Give the extent of all Plasmodium malariae-infected red blood cells.
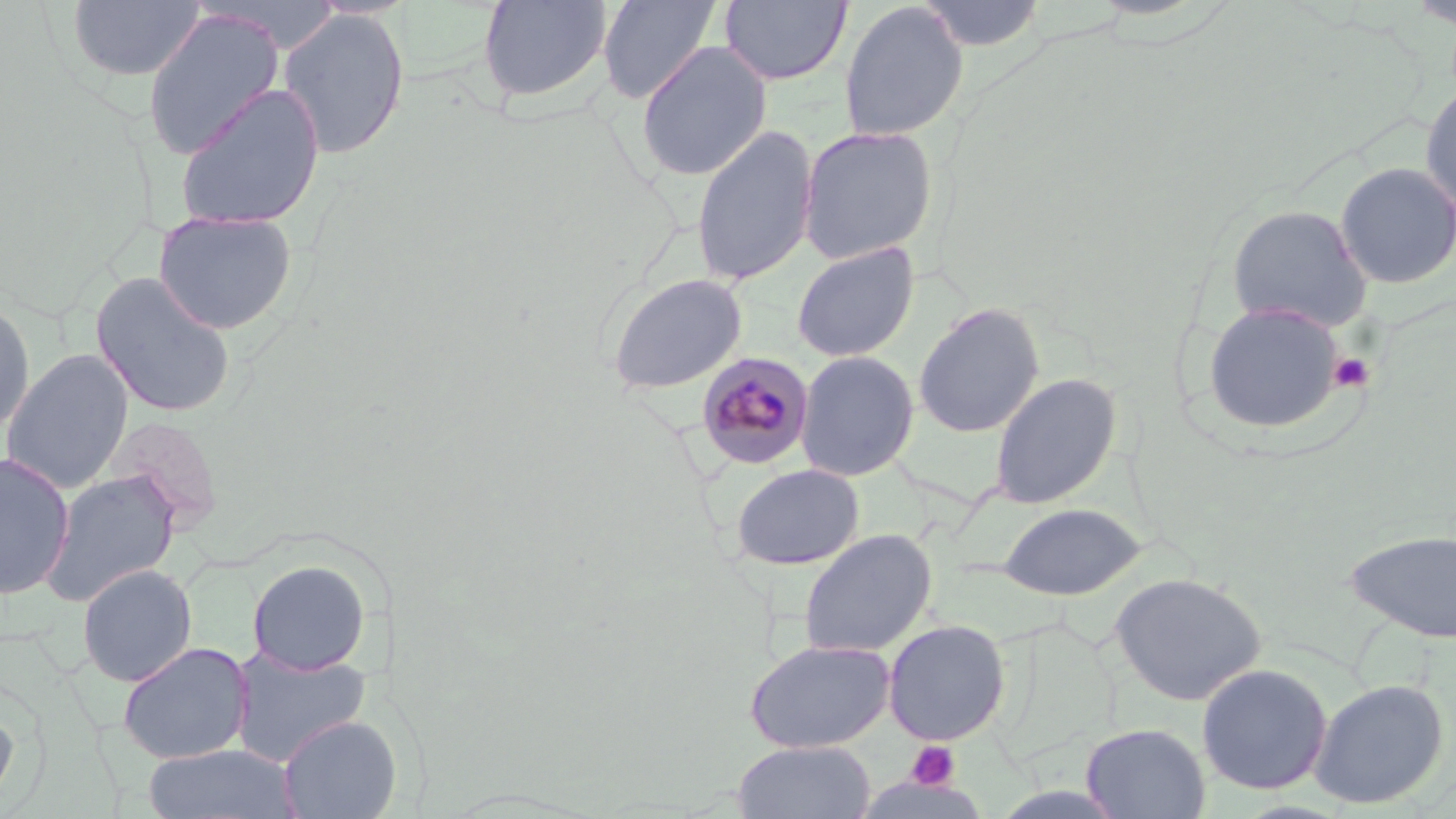

Approximate bounding boxes as named x1/y1/x2/y2 corners in pixels.
Plasmodium malariae-infected red blood cells: (x1=696, y1=351, x2=815, y2=470).

Summary:
  - Platelet locations: (x1=1328, y1=352, x2=1375, y2=393), (x1=906, y1=741, x2=961, y2=790)
  - Uninfected red blood cell locations: (x1=477, y1=0, x2=613, y2=105), (x1=596, y1=0, x2=723, y2=103), (x1=719, y1=0, x2=852, y2=86), (x1=918, y1=0, x2=1047, y2=52), (x1=66, y1=1, x2=206, y2=83), (x1=838, y1=1, x2=969, y2=142), (x1=277, y1=7, x2=410, y2=159), (x1=141, y1=8, x2=284, y2=160), (x1=635, y1=42, x2=773, y2=181), (x1=1420, y1=79, x2=1456, y2=215), (x1=173, y1=82, x2=325, y2=232), (x1=691, y1=123, x2=819, y2=286), (x1=798, y1=124, x2=938, y2=264), (x1=1334, y1=161, x2=1456, y2=289), (x1=1225, y1=203, x2=1373, y2=331), (x1=153, y1=209, x2=297, y2=334), (x1=791, y1=242, x2=920, y2=362), (x1=91, y1=271, x2=237, y2=418), (x1=605, y1=271, x2=748, y2=394), (x1=0, y1=296, x2=36, y2=438), (x1=1201, y1=299, x2=1347, y2=436), (x1=912, y1=303, x2=1045, y2=438), (x1=1, y1=349, x2=134, y2=494), (x1=795, y1=351, x2=920, y2=481), (x1=989, y1=373, x2=1122, y2=509), (x1=0, y1=452, x2=75, y2=599), (x1=729, y1=463, x2=865, y2=570), (x1=40, y1=469, x2=180, y2=607), (x1=996, y1=502, x2=1149, y2=600), (x1=1345, y1=527, x2=1456, y2=643), (x1=798, y1=528, x2=936, y2=658), (x1=248, y1=558, x2=371, y2=675), (x1=78, y1=564, x2=197, y2=686), (x1=1110, y1=571, x2=1268, y2=706), (x1=883, y1=619, x2=1011, y2=746), (x1=744, y1=638, x2=895, y2=753), (x1=117, y1=642, x2=254, y2=763), (x1=229, y1=645, x2=372, y2=767), (x1=1196, y1=662, x2=1333, y2=795), (x1=1308, y1=678, x2=1450, y2=810), (x1=0, y1=694, x2=19, y2=811), (x1=278, y1=714, x2=402, y2=819), (x1=1080, y1=722, x2=1211, y2=819), (x1=733, y1=740, x2=877, y2=819), (x1=141, y1=743, x2=301, y2=819)
  - Slide-level diagnosis: Plasmodium malariae
  - Preparation: thin blood smear
  - Modality: light microscopy
  - Field of view: one of a larger specimen
  - Image size: 1456×819 pixels
  - Magnification: 1000x
  - Stain: May-Grünwald-Giemsa